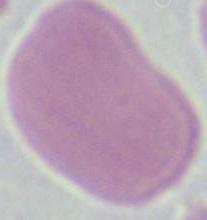

Captured at 1000x magnification. Micrograph. An erythrocyte is seen.